Give the extent of all Plasmodium falciparum-infected red blood cells.
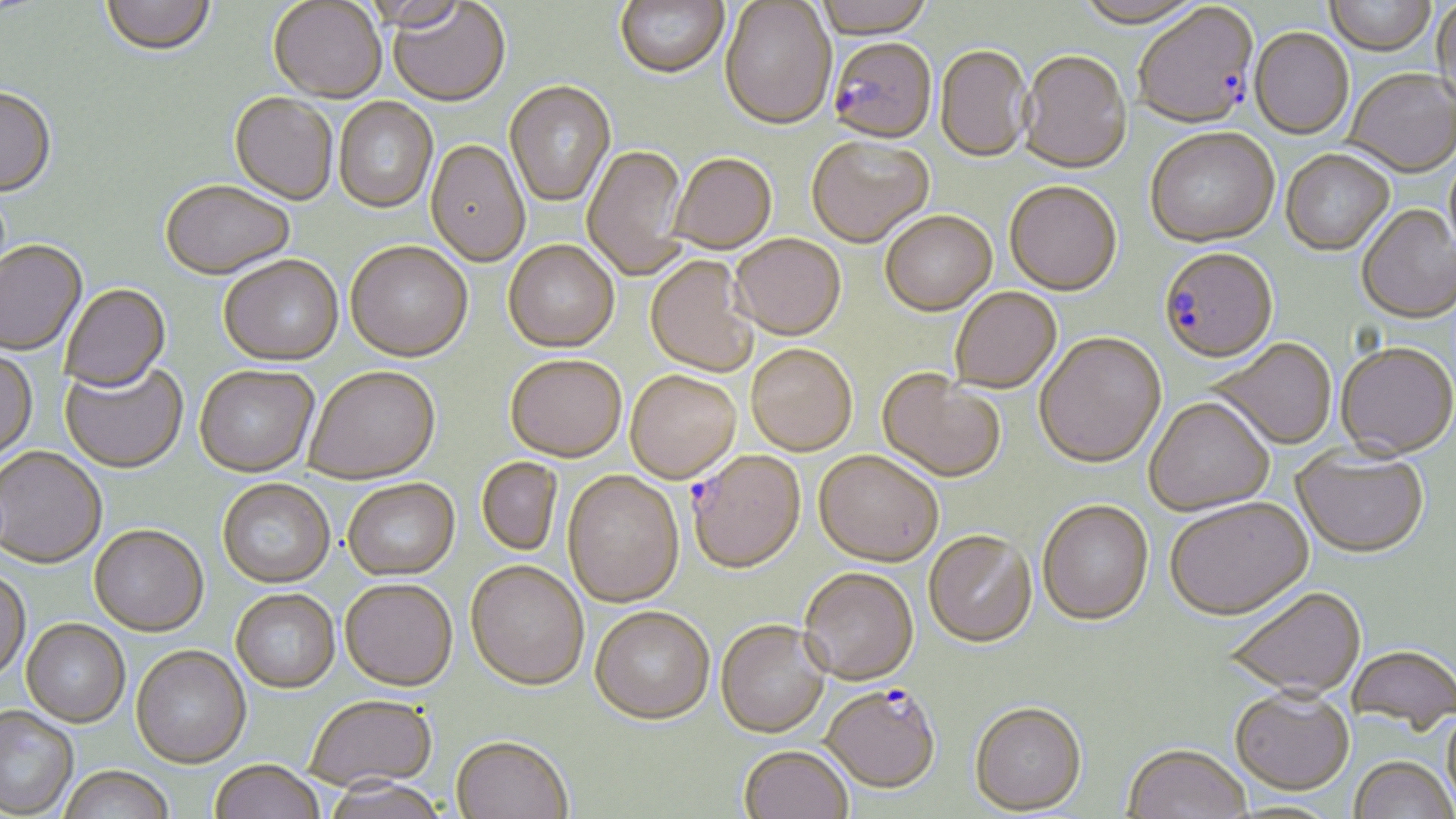
Approximate bounding boxes as (x1, y1, x2, y2) in pixels.
Plasmodium falciparum-infected red blood cells: (1134, 5, 1258, 131), (828, 40, 938, 146), (1159, 250, 1278, 365), (689, 452, 806, 575), (820, 685, 940, 797).

slide-level diagnosis = Plasmodium falciparum
field of view = single
preparation = thin blood smear
magnification = 1000x
uninfected red blood cell locations = approximate bounding boxes as (x1, y1, x2, y2) in pixels: (101, 0, 216, 56), (614, 0, 729, 80), (812, 0, 935, 40), (1323, 0, 1437, 57), (1432, 0, 1455, 109), (268, 1, 387, 102), (388, 2, 510, 107), (719, 2, 837, 132), (1074, 2, 1206, 30), (1249, 30, 1354, 142), (935, 46, 1033, 165), (1018, 52, 1131, 176), (1344, 71, 1456, 180), (504, 82, 616, 208), (0, 88, 57, 199), (228, 93, 338, 206), (334, 98, 438, 214), (1146, 131, 1279, 249), (806, 137, 934, 250), (425, 140, 530, 268), (582, 145, 689, 281), (1281, 152, 1394, 257), (668, 154, 777, 255), (160, 181, 294, 280), (1004, 183, 1122, 298), (1357, 206, 1456, 326), (880, 213, 997, 318), (731, 235, 846, 341), (504, 240, 619, 353), (345, 241, 473, 363), (0, 242, 87, 357), (219, 256, 343, 366), (646, 257, 757, 378), (59, 284, 171, 394), (951, 289, 1062, 395), (1035, 334, 1166, 469), (1210, 340, 1336, 451), (1336, 344, 1456, 460), (746, 345, 857, 457), (0, 350, 38, 463), (505, 356, 626, 463), (59, 360, 188, 473), (194, 364, 319, 477), (304, 366, 440, 484), (877, 371, 1006, 484), (625, 372, 741, 484), (1144, 399, 1274, 516), (0, 447, 107, 569), (1292, 448, 1429, 559), (813, 451, 943, 567), (477, 457, 562, 556), (563, 472, 684, 608), (218, 479, 335, 588), (343, 479, 460, 581), (1165, 498, 1313, 622), (1038, 501, 1154, 627), (89, 525, 208, 637), (923, 531, 1036, 650), (466, 562, 588, 693), (799, 568, 918, 686), (0, 570, 31, 684), (340, 581, 457, 693), (1223, 587, 1367, 700), (231, 589, 341, 694), (589, 607, 714, 726), (21, 620, 130, 728), (715, 621, 830, 740), (1346, 645, 1455, 735), (131, 647, 251, 770), (1229, 688, 1354, 796), (306, 696, 437, 795), (968, 702, 1087, 816), (1441, 703, 1456, 816), (0, 708, 78, 818), (450, 738, 573, 819), (1122, 745, 1252, 819), (738, 747, 853, 819), (1349, 757, 1454, 818), (209, 762, 325, 819), (57, 769, 175, 819), (322, 779, 449, 819)
stain = May-Grünwald-Giemsa
modality = light microscopy
image size = 1456×819 pixels